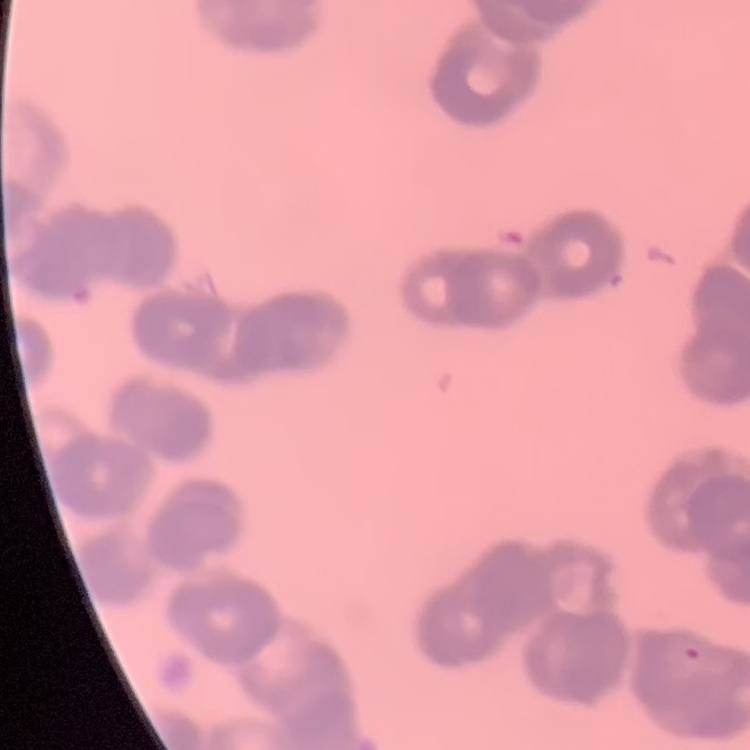

Summary:
  - Erythrocyte morphology: rouleaux formation
  - Preparation: thin peripheral smear
  - Stain: Field's or Giemsa
  - Image type: one tile cut from a larger photomicrograph